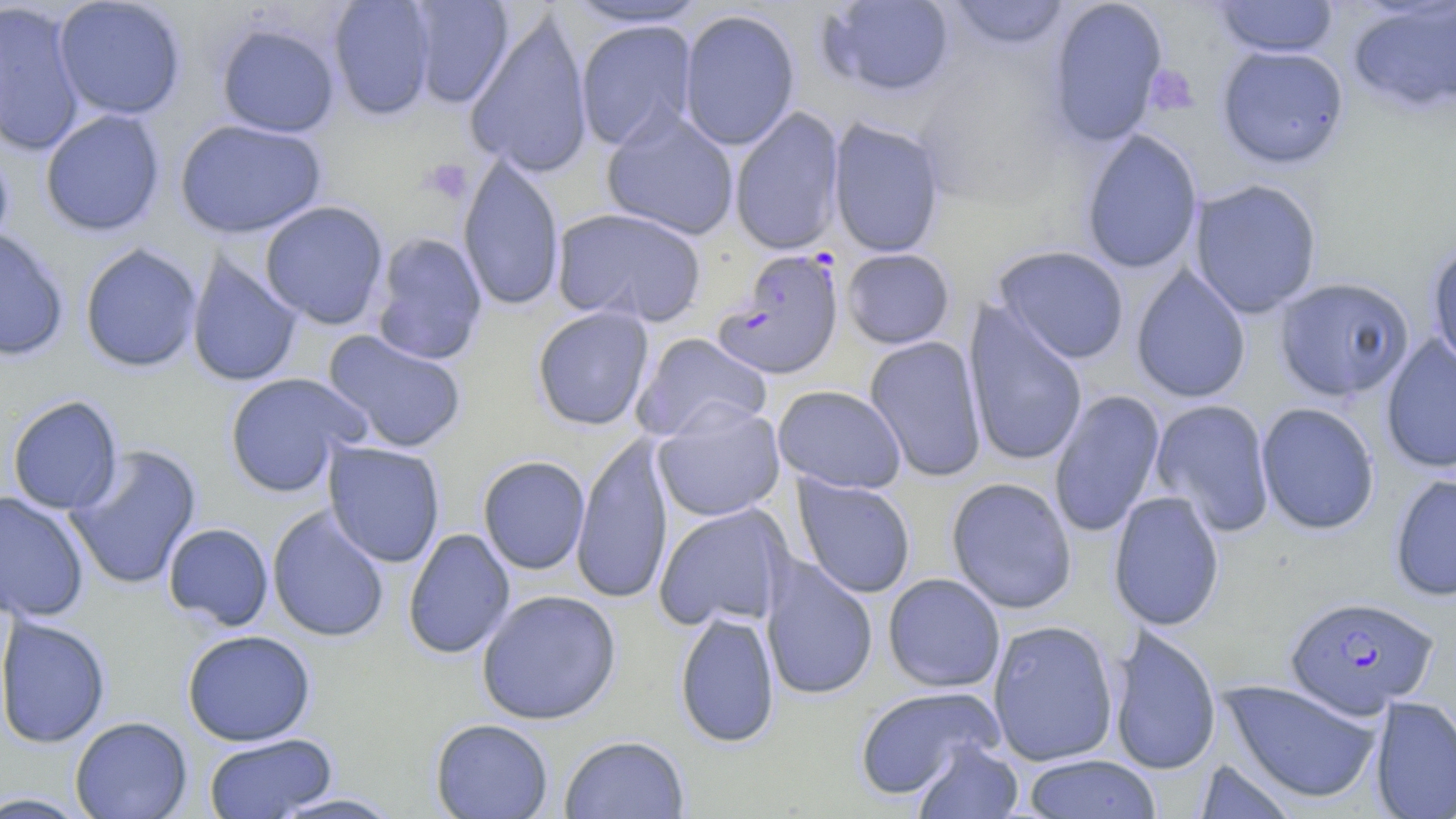
Approximate bounding boxes as (x1, y1, x2, y2) in pixels. Platelet locations: (1145, 66, 1198, 116), (421, 160, 472, 204). Plasmodium falciparum-infected red blood cell locations: (712, 248, 845, 381), (1285, 595, 1438, 717). Uninfected red blood cell locations: (53, 0, 187, 120), (328, 0, 436, 120), (405, 0, 514, 108), (561, 0, 712, 29), (818, 0, 956, 98), (946, 0, 1071, 50), (1045, 0, 1169, 147), (1211, 0, 1340, 58), (0, 1, 86, 157), (1346, 1, 1456, 116), (677, 9, 801, 150), (464, 10, 595, 179), (574, 19, 698, 152), (215, 22, 340, 138), (1216, 44, 1350, 169), (729, 106, 845, 256), (600, 108, 740, 241), (40, 109, 165, 237), (827, 117, 946, 258), (174, 119, 327, 239), (1080, 128, 1203, 274), (0, 140, 15, 262), (457, 154, 565, 313), (1188, 178, 1323, 318), (259, 200, 389, 329), (551, 206, 708, 328), (0, 227, 70, 362), (370, 232, 488, 366), (1425, 239, 1456, 373), (79, 242, 203, 373), (993, 245, 1130, 364), (841, 248, 955, 349), (186, 252, 304, 388), (1130, 264, 1252, 404), (1274, 277, 1415, 401), (963, 302, 1088, 469), (532, 306, 655, 431), (322, 330, 467, 454), (631, 332, 773, 443), (1381, 335, 1456, 474), (864, 336, 988, 483), (223, 372, 369, 498), (772, 384, 907, 493), (1048, 389, 1166, 538), (7, 395, 123, 515), (1150, 398, 1276, 537), (652, 400, 786, 522), (1255, 401, 1381, 535), (571, 433, 674, 604), (323, 440, 446, 568), (64, 443, 203, 591), (478, 455, 590, 575), (1389, 472, 1456, 602), (792, 475, 917, 599), (945, 476, 1078, 614), (1107, 490, 1225, 631), (0, 491, 91, 623), (653, 503, 793, 631), (267, 506, 390, 643), (163, 522, 274, 631), (403, 528, 516, 660), (760, 556, 879, 701), (883, 573, 1005, 693), (476, 589, 622, 725), (675, 609, 780, 748), (1, 614, 112, 749), (988, 619, 1119, 767), (1107, 624, 1222, 777), (181, 629, 317, 746), (1220, 678, 1383, 804), (854, 686, 1005, 800), (1370, 695, 1456, 819), (70, 716, 193, 819), (430, 718, 554, 818), (203, 733, 337, 818), (559, 735, 690, 818), (911, 740, 1024, 818), (1022, 754, 1162, 819), (1193, 757, 1300, 819), (267, 791, 406, 818), (0, 792, 93, 818). Slide-level diagnosis: Plasmodium falciparum. Single field of view. Optical microscopy. Thin blood film. Image is 1456×819 pixels. 1000x magnification. May-Grünwald-Giemsa stain.